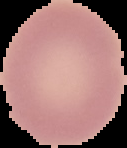

Summary:
  - Preparation: thin blood film
  - Result: no malaria parasites detected
  - Image type: segmented cell region on a black background
  - Image size: 127×148 pixels